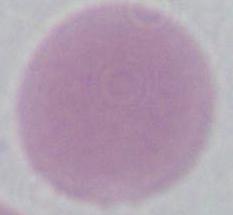
Summary:
  - Modality: photomicrograph
  - Magnification: 1000x
  - Identification: red blood cell